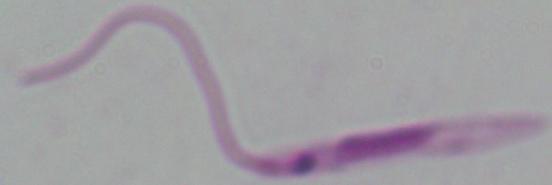
{
  "identification": "Leishmania",
  "modality": "photomicrograph",
  "magnification": "1000x"
}